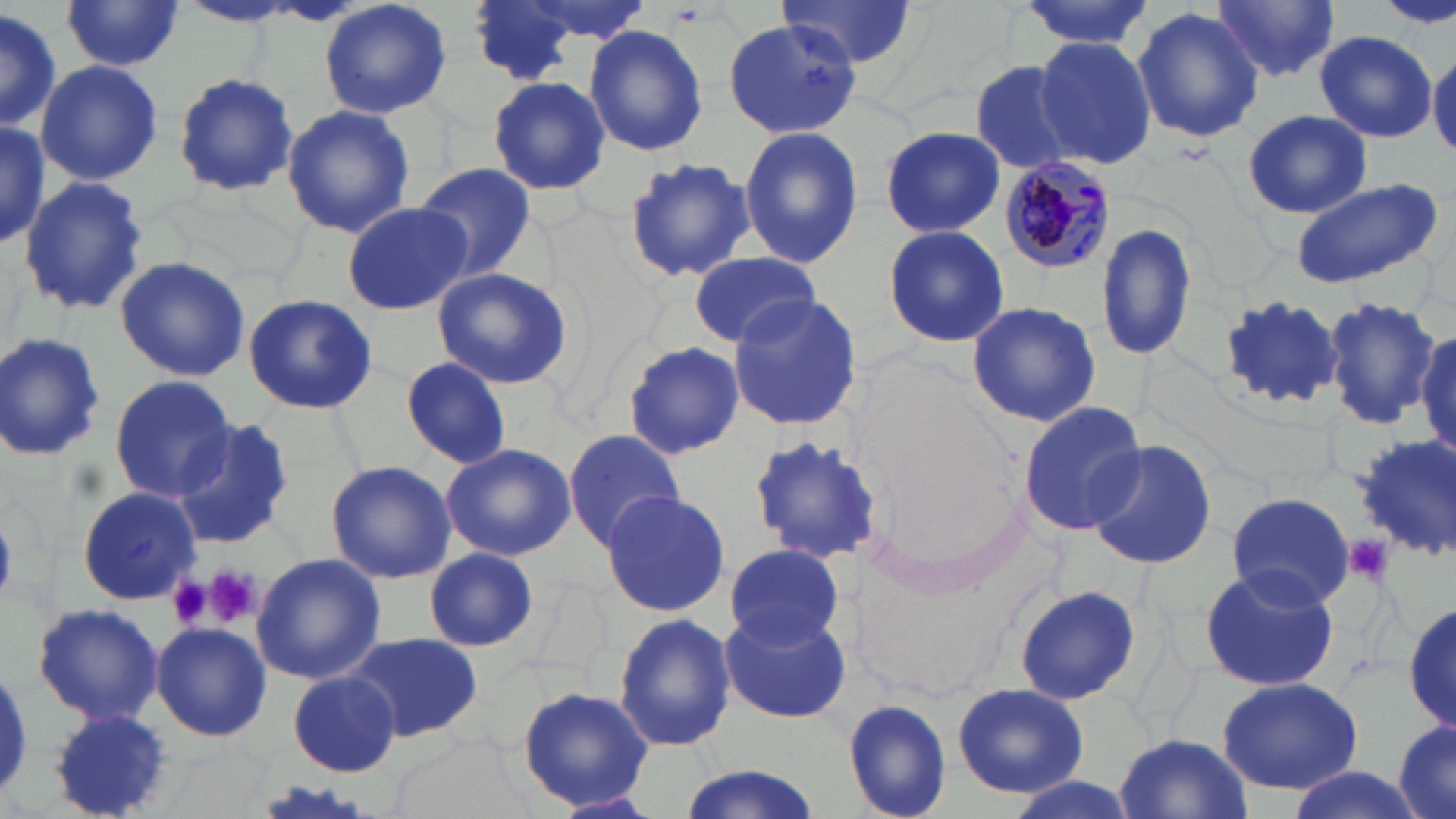
Summary:
  - Coordinate format: approximate bounding boxes as (x1, y1, x2, y2) in pixels
  - Uninfected red blood cell locations: (320, 0, 452, 120), (464, 0, 588, 87), (773, 0, 917, 71), (1014, 0, 1154, 50), (1379, 0, 1454, 27), (62, 1, 184, 71), (1212, 1, 1341, 81), (182, 3, 295, 28), (0, 7, 61, 132), (1132, 7, 1264, 143), (722, 20, 860, 138), (583, 23, 708, 159), (1314, 32, 1436, 140), (1032, 37, 1159, 169), (1428, 51, 1456, 157), (969, 58, 1084, 176), (36, 60, 163, 187), (174, 70, 300, 197), (486, 76, 611, 196), (282, 103, 415, 240), (1243, 110, 1376, 220), (0, 118, 49, 249), (876, 126, 1008, 239), (737, 127, 863, 267), (627, 158, 757, 282), (413, 162, 538, 279), (19, 176, 149, 318), (1289, 177, 1447, 291), (341, 201, 472, 315), (1095, 219, 1199, 365), (882, 223, 1010, 349), (687, 251, 820, 347), (116, 256, 251, 382), (430, 267, 574, 389), (243, 294, 376, 415), (726, 295, 865, 431), (1216, 295, 1347, 411), (1320, 296, 1443, 428), (966, 301, 1102, 429), (1412, 326, 1455, 464), (0, 332, 107, 464), (623, 342, 742, 461), (401, 357, 513, 467), (110, 375, 234, 502), (1018, 401, 1146, 538), (170, 419, 294, 548), (563, 431, 687, 548), (748, 433, 882, 567), (1084, 439, 1218, 572), (441, 442, 577, 561), (327, 460, 455, 583), (77, 486, 199, 604), (599, 491, 731, 616), (1226, 493, 1354, 609), (725, 545, 845, 649), (424, 547, 538, 651), (251, 552, 386, 685), (1197, 565, 1340, 692), (1015, 583, 1139, 705), (1405, 602, 1456, 733), (35, 603, 163, 726), (721, 610, 850, 724), (613, 612, 736, 753), (152, 623, 271, 741), (349, 633, 482, 743), (288, 672, 399, 775), (1216, 678, 1364, 793), (952, 682, 1092, 800), (516, 683, 656, 813), (842, 698, 953, 819), (49, 710, 176, 819), (1392, 716, 1456, 819), (1114, 732, 1253, 819), (672, 764, 826, 819), (1281, 769, 1428, 819)
  - Plasmodium malariae-infected red blood cell locations: (997, 156, 1116, 275)
  - Platelet locations: (1342, 534, 1395, 588), (205, 565, 261, 628), (165, 576, 211, 629)
  - Slide-level diagnosis: Plasmodium malariae
  - Magnification: 1000x
  - Field of view: single
  - Modality: light microscopy
  - Image size: 1456×819 pixels
  - Stain: May-Grünwald-Giemsa
  - Preparation: thin blood film